Point out each Plasmodium parasite.
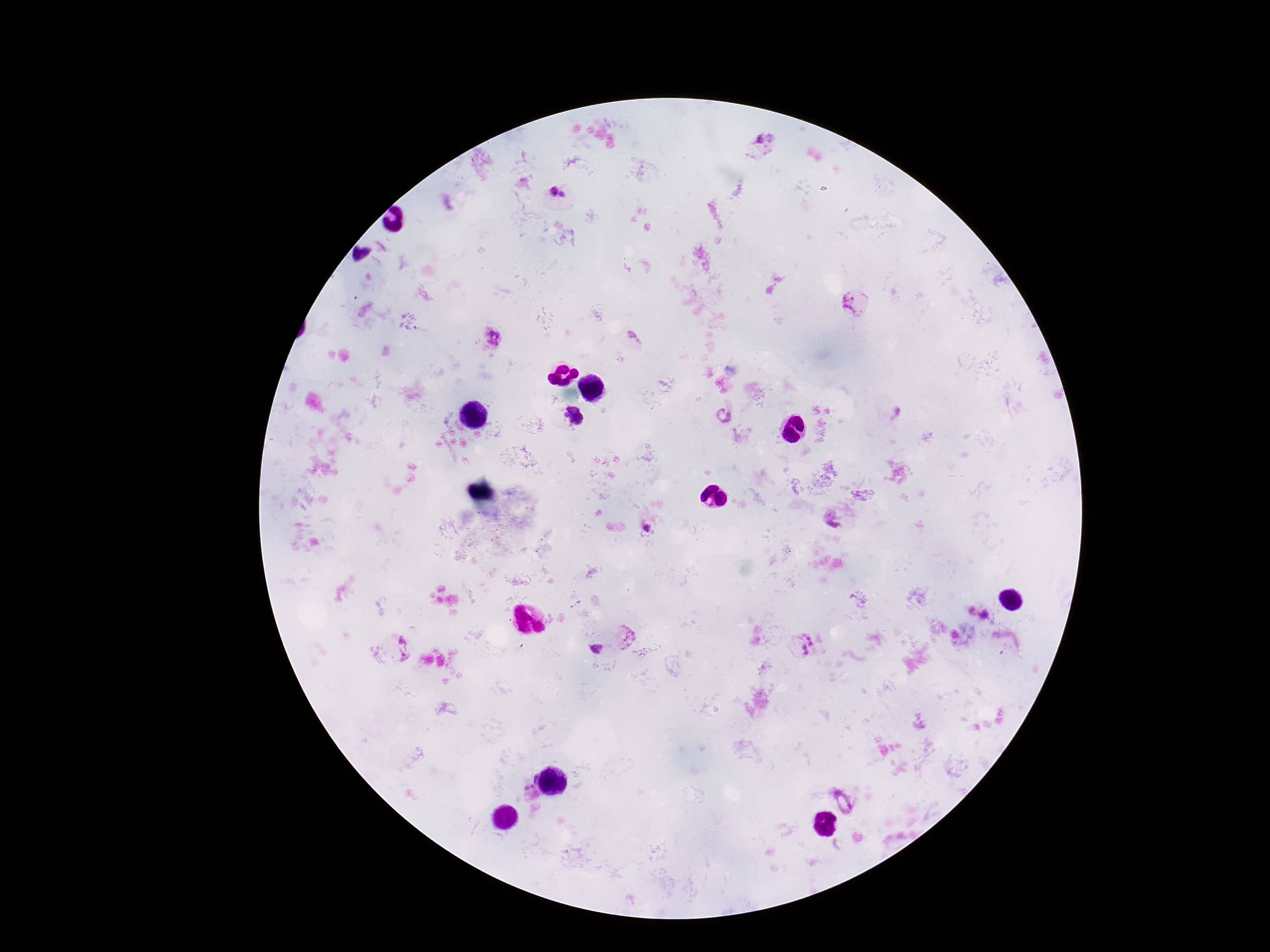
Approximate object centers, in pixels from the top-left corner.
Plasmodium parasites: (x=766, y=141), (x=553, y=191), (x=564, y=195), (x=850, y=303), (x=494, y=337), (x=634, y=337), (x=573, y=416), (x=726, y=417), (x=834, y=519), (x=646, y=530), (x=972, y=612), (x=985, y=614), (x=403, y=641), (x=805, y=645), (x=594, y=649), (x=405, y=658), (x=529, y=780), (x=844, y=802).

preparation = thick blood film
magnification = 100x
field of view = single
image size = 1270×952 pixels
patient malaria status = positive
stain = Giemsa
capture = smartphone camera through the microscope eyepiece